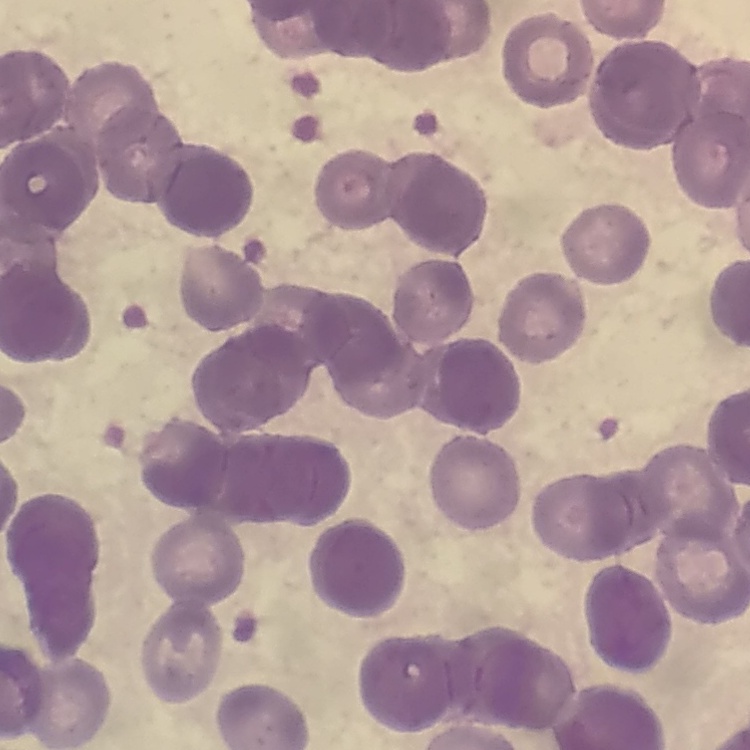

Summary:
  - Red blood cell morphology: rouleaux formation
  - Preparation: thin blood smear
  - Image type: square crop of a larger photomicrograph
  - Stain: Field's or Giemsa